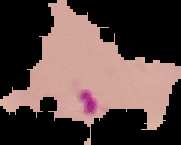
Result: malaria parasites identified. Image is 181×145 pixels. Segmented cell region on a black background. From a thin blood smear.